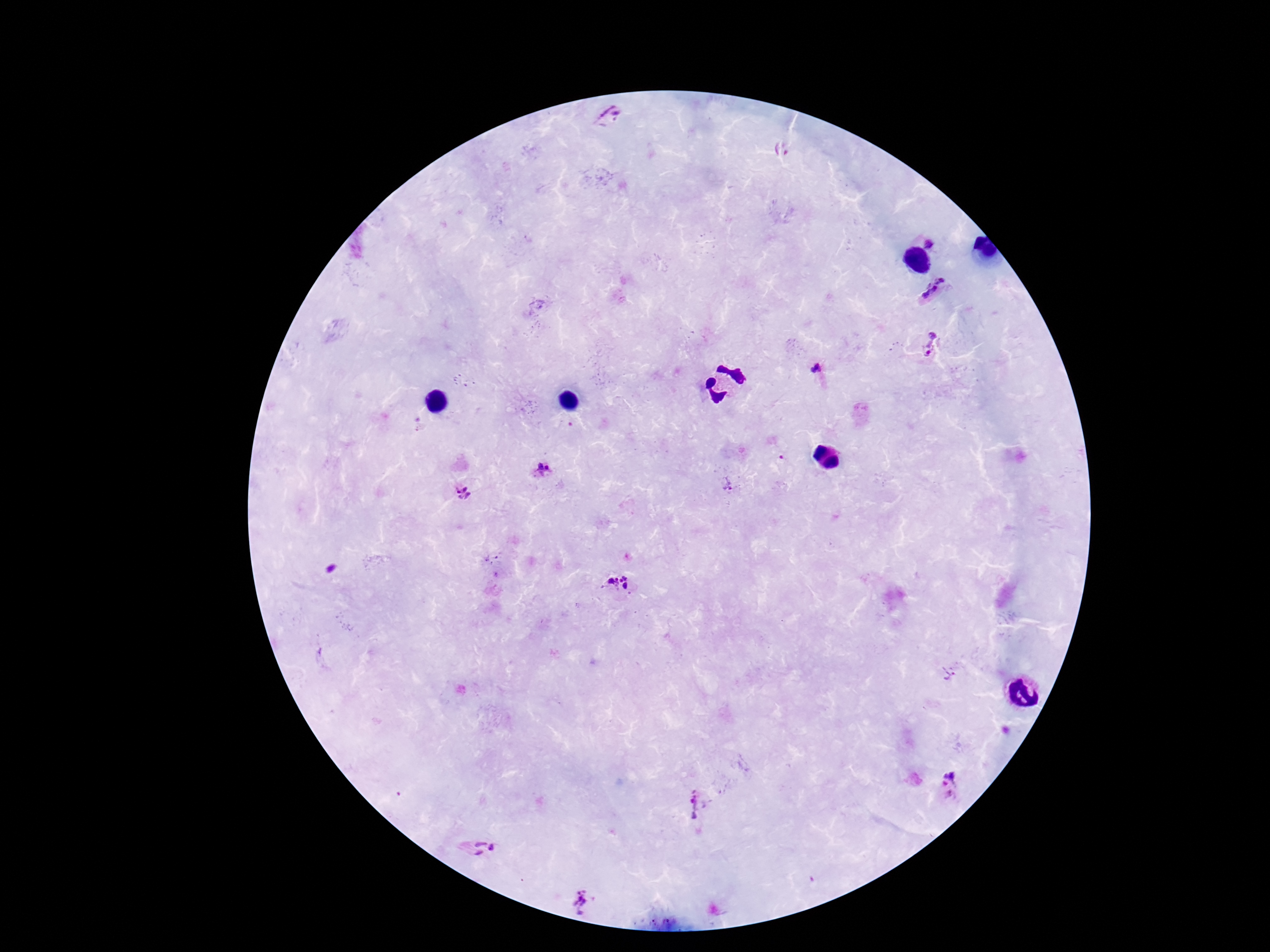
Approximate centers as [x, y] in pixels.
Summary:
  - Plasmodium parasite locations: [609, 123], [931, 242], [938, 291], [929, 345], [818, 369], [542, 469], [462, 494], [623, 578], [617, 579], [609, 581], [626, 586], [949, 672], [952, 783], [697, 804], [481, 849], [581, 902]
  - Capture: smartphone camera through the microscope eyepiece
  - Preparation: thick blood film
  - Field of view: one from this slide
  - Stain: Giemsa
  - Image size: 1270×952 pixels
  - Magnification: 100x
  - Patient malaria status: positive